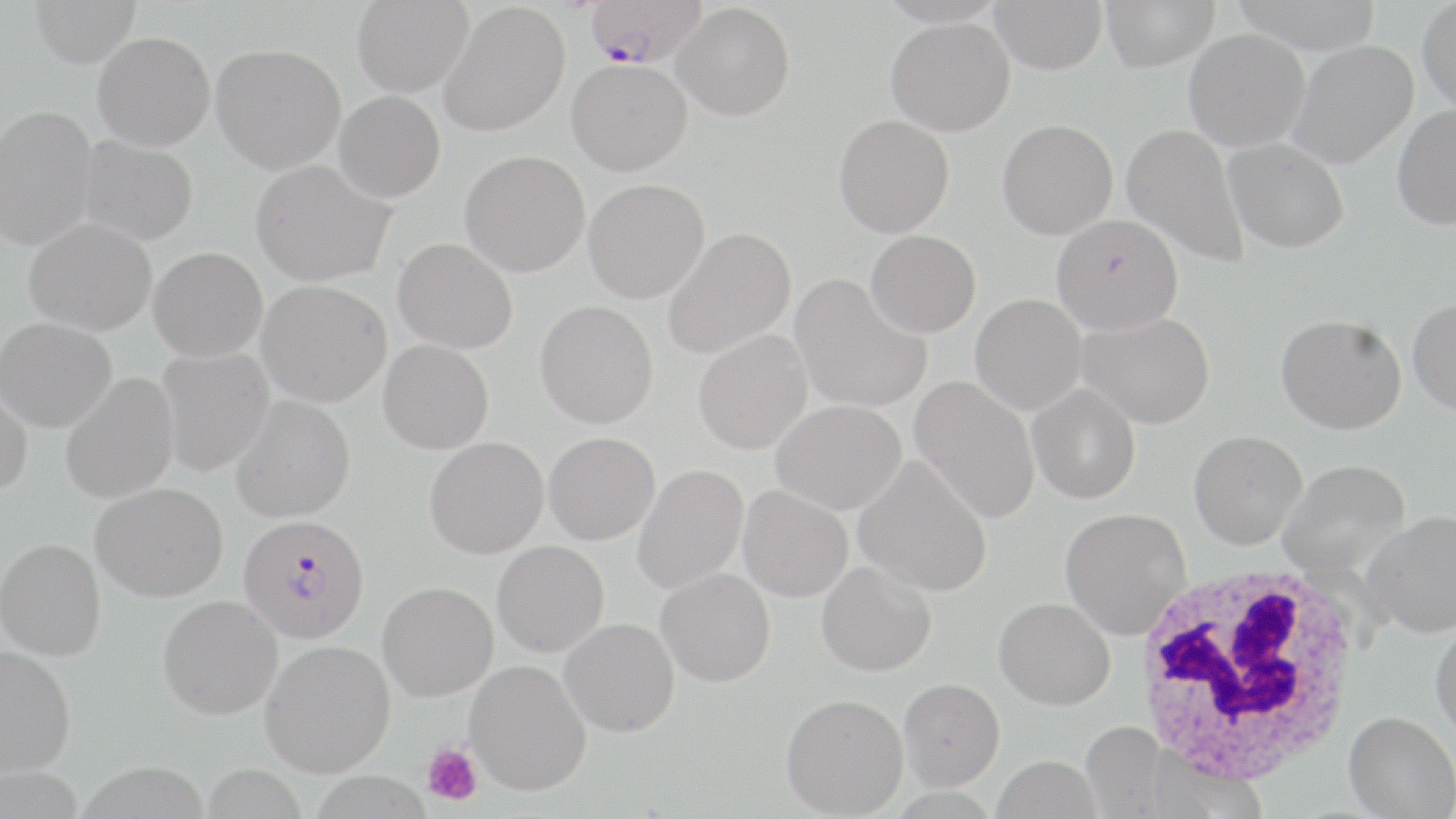
slide-level diagnosis = Plasmodium falciparum
image size = 1456×819 pixels
white blood cell locations = approximate bounding boxes as (x1, y1, x2, y2) in pixels: (1132, 560, 1366, 786)
magnification = 1000x
uninfected red blood cell locations = approximate bounding boxes as (x1, y1, x2, y2) in pixels: (29, 0, 141, 67), (352, 0, 474, 98), (990, 0, 1107, 75), (1100, 0, 1220, 71), (1230, 0, 1384, 55), (1417, 0, 1456, 115), (440, 2, 570, 136), (672, 3, 795, 121), (886, 17, 1015, 136), (1184, 28, 1311, 151), (93, 31, 215, 151), (1287, 39, 1419, 169), (211, 43, 346, 174), (567, 58, 692, 176), (334, 91, 445, 203), (1391, 103, 1456, 230), (0, 105, 98, 249), (834, 115, 954, 238), (997, 119, 1118, 240), (1122, 123, 1249, 268), (78, 136, 199, 246), (1224, 138, 1349, 254), (460, 150, 590, 276), (251, 160, 394, 286), (584, 179, 710, 303), (1052, 214, 1183, 333), (24, 218, 156, 336), (663, 227, 796, 359), (865, 230, 981, 338), (393, 238, 518, 353), (148, 246, 267, 361), (791, 274, 932, 414), (256, 280, 391, 407), (970, 294, 1086, 415), (1408, 297, 1456, 416), (535, 300, 658, 428), (1078, 311, 1215, 429), (1276, 314, 1406, 435), (0, 317, 117, 432), (694, 330, 813, 454), (378, 340, 494, 454), (156, 349, 275, 476), (60, 373, 179, 504), (911, 376, 1040, 524), (0, 381, 33, 499), (1027, 383, 1140, 504), (231, 395, 355, 522), (771, 399, 906, 515), (1189, 430, 1307, 549), (544, 432, 660, 545), (425, 437, 549, 559), (853, 455, 992, 597), (1278, 459, 1411, 577), (632, 464, 749, 595), (91, 482, 228, 602), (738, 485, 853, 603), (1060, 507, 1191, 639), (1362, 511, 1456, 637), (0, 538, 105, 659), (492, 540, 609, 657), (816, 561, 937, 677), (656, 568, 776, 686), (377, 581, 498, 702), (158, 595, 282, 719), (994, 597, 1115, 710), (560, 618, 680, 737), (1431, 621, 1456, 743), (261, 639, 395, 776), (0, 645, 76, 777), (465, 660, 592, 795), (898, 678, 1005, 790), (780, 693, 908, 818), (1343, 711, 1456, 818), (1080, 721, 1170, 818), (1144, 749, 1268, 818), (991, 755, 1102, 818)
field of view = single
platelet locations = approximate bounding boxes as (x1, y1, x2, y2) in pixels: (422, 742, 483, 805)
Plasmodium falciparum-infected red blood cell locations = approximate bounding boxes as (x1, y1, x2, y2) in pixels: (586, 0, 707, 68), (238, 514, 370, 644)
preparation = thin blood film
stain = May-Grünwald-Giemsa
modality = optical microscopy